State which parasite is depicted.
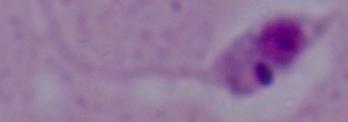
This is Leishmania.

1000x magnification. Micrograph.